Assess this cell for malaria.
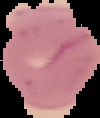

It is parasitized.

From a thin blood smear. Image is 100×118 pixels. Cell region segmented out of the field of view; the surrounding area is masked to black.